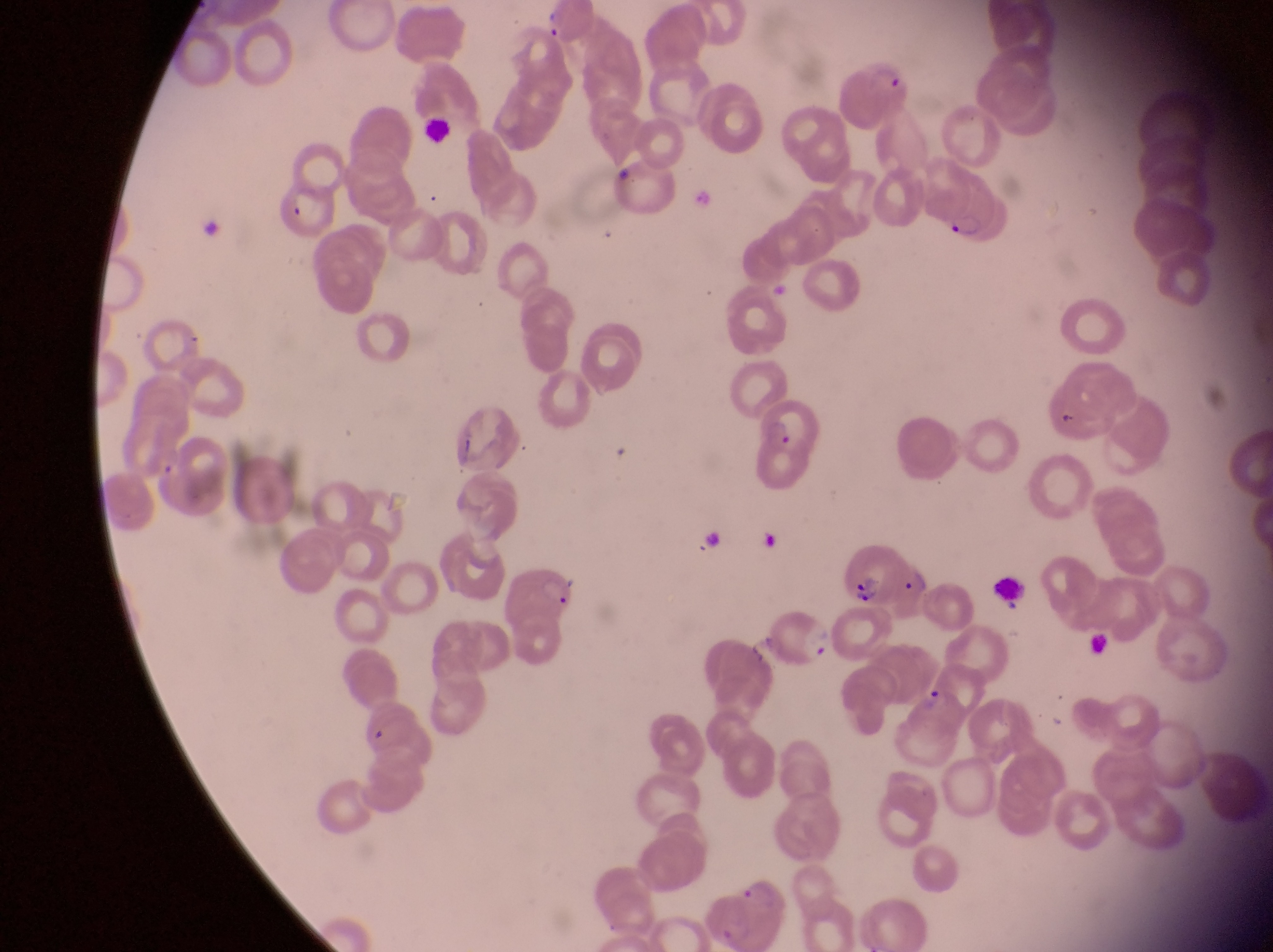
trophozoite locations = approximate bounding boxes as (left, top, right, bottom) in pixels: (917, 683, 953, 715)
capture = smartphone photograph through the eyepiece of an Olympus CX-23 microscope
field of view = single
leukocyte locations = approximate bounding boxes as (left, top, right, bottom) in pixels: (995, 571, 1034, 616)
magnification = 1000x
image size = 1273×952 pixels
preparation = thin blood smear
country = Uganda
parasitised red blood cell locations = approximate bounding boxes as (left, top, right, bottom) in pixels: (845, 51, 915, 121), (914, 150, 999, 250), (268, 176, 334, 237), (752, 400, 827, 458), (838, 545, 901, 605), (902, 556, 933, 625), (766, 607, 840, 674)